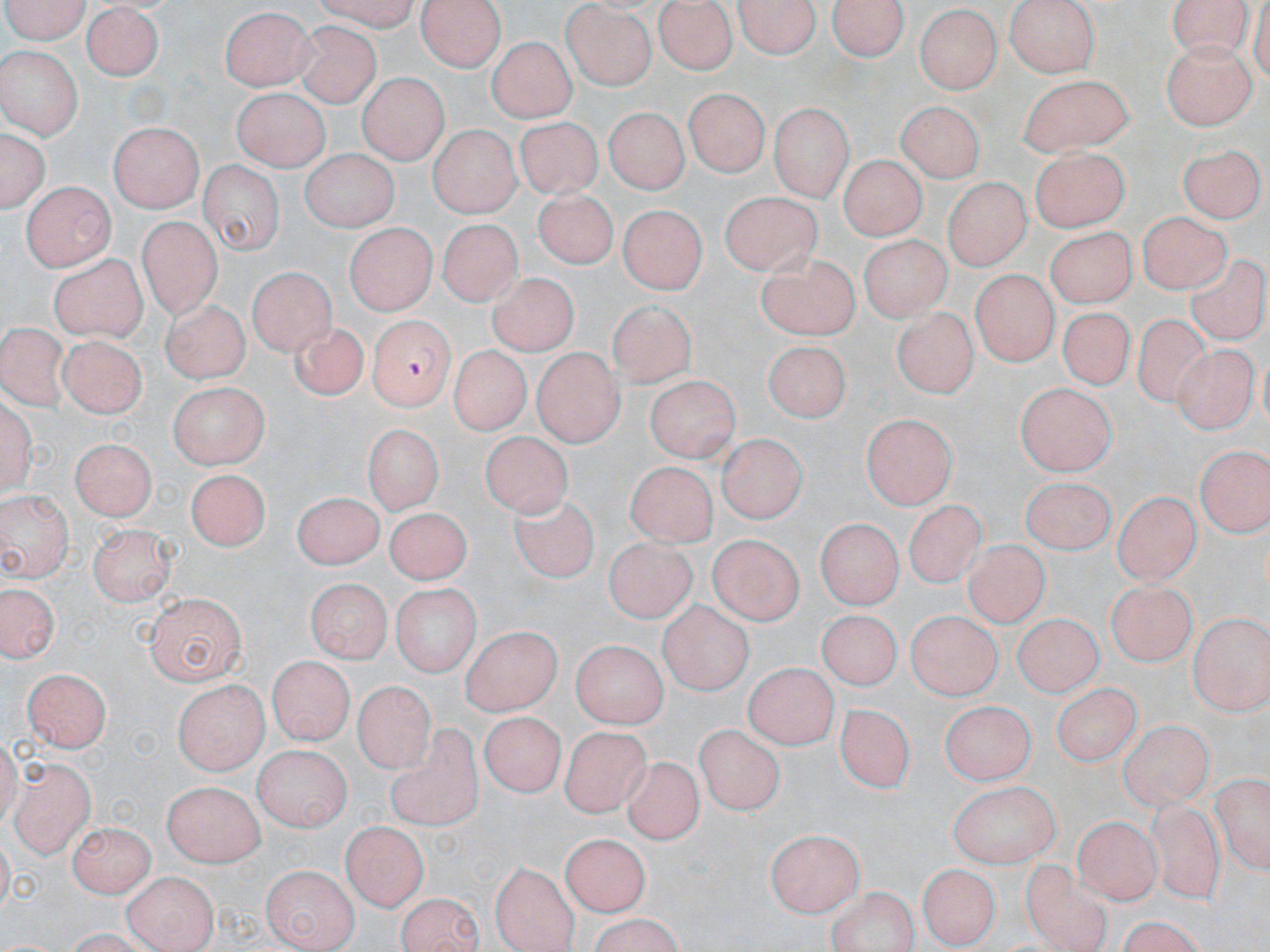

Summary:
  - Coordinate format: approximate bounding boxes as (x1, y1, x2, y2) in pixels
  - Plasmodium falciparum-infected red blood cell locations: (368, 319, 456, 410)
  - Uninfected red blood cell locations: (1, 0, 96, 41), (314, 0, 422, 31), (737, 0, 819, 62), (830, 0, 906, 64), (1003, 0, 1102, 76), (1165, 0, 1252, 53), (420, 1, 505, 72), (654, 1, 738, 74), (82, 4, 163, 83), (560, 5, 656, 88), (222, 6, 316, 91), (913, 8, 998, 94), (289, 21, 381, 108), (486, 38, 581, 120), (1158, 41, 1257, 129), (0, 46, 83, 138), (1019, 71, 1132, 155), (357, 72, 447, 163), (684, 87, 768, 176), (232, 88, 330, 169), (768, 102, 849, 200), (897, 102, 984, 182), (603, 107, 685, 194), (516, 119, 607, 203), (109, 123, 203, 212), (430, 126, 518, 217), (2, 127, 47, 213), (1029, 145, 1131, 233), (1181, 145, 1262, 222), (297, 151, 400, 231), (837, 155, 922, 241), (199, 162, 281, 253), (20, 181, 113, 269), (532, 181, 622, 268), (941, 182, 1030, 270), (721, 191, 819, 273), (619, 202, 709, 293), (1135, 208, 1224, 289), (139, 217, 218, 319), (433, 220, 529, 308), (1048, 225, 1134, 309), (342, 227, 433, 316), (862, 236, 949, 321), (48, 255, 146, 342), (755, 256, 862, 341), (1188, 257, 1265, 340), (249, 263, 337, 352), (971, 265, 1061, 367), (485, 275, 579, 356), (163, 299, 250, 381), (605, 300, 695, 390), (894, 304, 974, 397), (1055, 307, 1136, 392), (1135, 312, 1217, 410), (0, 319, 66, 408), (289, 321, 371, 401), (57, 336, 145, 420), (764, 341, 851, 422), (1173, 345, 1254, 433), (450, 346, 526, 435), (531, 350, 624, 443), (645, 375, 738, 461), (170, 382, 265, 470), (1015, 382, 1119, 477), (862, 416, 958, 507), (360, 422, 445, 514), (717, 431, 804, 523), (482, 433, 578, 523), (73, 435, 155, 519), (1197, 445, 1267, 539), (623, 457, 713, 542), (185, 468, 269, 553), (1017, 473, 1115, 555), (0, 486, 75, 582), (1111, 491, 1203, 585), (291, 492, 383, 568), (511, 492, 604, 583), (907, 502, 983, 587), (381, 509, 474, 586), (818, 515, 906, 607), (87, 523, 177, 607), (707, 532, 802, 628), (604, 537, 698, 624), (961, 539, 1047, 628), (306, 573, 390, 656), (1104, 579, 1194, 667), (2, 580, 60, 667), (391, 580, 479, 677), (142, 593, 245, 681), (660, 601, 750, 695), (813, 608, 899, 689), (902, 611, 1003, 699), (1011, 611, 1101, 699), (1189, 611, 1268, 714), (458, 626, 562, 715), (571, 640, 668, 730), (265, 655, 354, 743), (743, 658, 834, 745), (21, 666, 111, 751), (172, 677, 271, 772), (355, 677, 431, 768), (1054, 681, 1143, 769), (941, 698, 1031, 787), (837, 702, 916, 791), (481, 712, 564, 793), (1120, 721, 1212, 805), (390, 724, 481, 834), (697, 724, 782, 817), (563, 729, 654, 824), (256, 744, 352, 828), (619, 753, 703, 848), (8, 761, 94, 856), (1207, 770, 1268, 874), (163, 779, 266, 864), (947, 780, 1061, 866), (1145, 798, 1228, 906), (1072, 816, 1159, 906), (70, 818, 152, 893), (342, 822, 426, 909), (764, 828, 864, 913), (561, 834, 650, 916), (1021, 858, 1112, 952), (488, 861, 576, 950), (261, 862, 357, 948), (915, 865, 998, 949), (121, 870, 215, 951), (828, 885, 916, 950), (397, 889, 482, 952), (585, 917, 691, 952)
  - Slide-level diagnosis: Plasmodium falciparum
  - Preparation: thin blood smear
  - Modality: light microscopy
  - Magnification: 1000x
  - Image size: 1270×952 pixels
  - Stain: May-Grünwald-Giemsa
  - Field of view: single